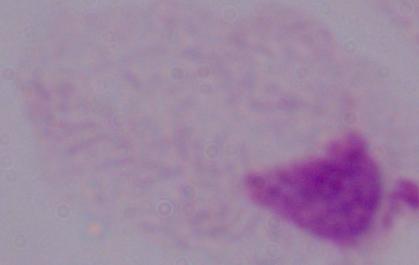

Summary:
  - Modality: photomicrograph
  - Identification: trichomonad
  - Magnification: 1000x